Name the parasite shown.
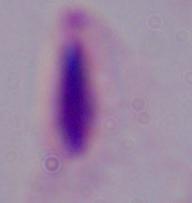
This is a trichomonad.

Summary:
  - Magnification: 1000x
  - Modality: photomicrograph